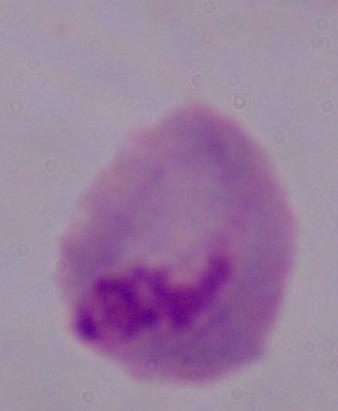
modality = micrograph
magnification = 1000x
identification = trichomonad